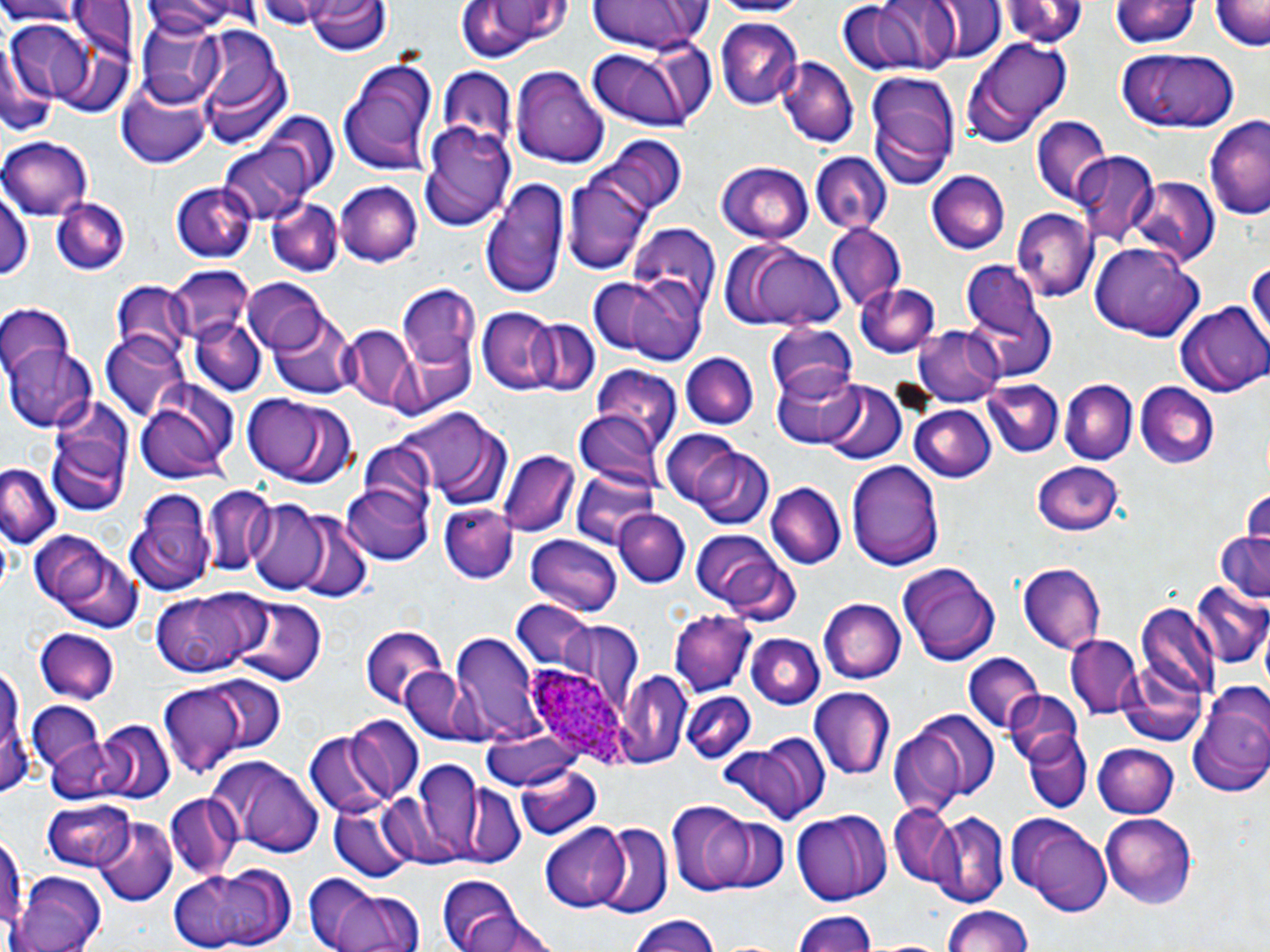
{
  "slide_level_diagnosis": "Plasmodium ovale",
  "magnification": "1000x",
  "plasmodium_ovale_infected_red_blood_cell_locations": "approximate bounding boxes as [x1, y1, x2, y2] in pixels: [526, 665, 626, 764]",
  "image_size": "1270×952 pixels",
  "uninfected_red_blood_cell_locations": "approximate bounding boxes as [x1, y1, x2, y2] in pixels: [0, 0, 86, 25], [258, 0, 322, 32], [583, 0, 715, 54], [703, 0, 813, 17], [839, 0, 963, 77], [136, 1, 258, 37], [305, 1, 389, 56], [450, 1, 570, 64], [932, 1, 1004, 65], [1002, 1, 1088, 51], [1111, 1, 1198, 52], [1212, 2, 1268, 51], [714, 15, 802, 108], [134, 19, 227, 104], [6, 22, 98, 100], [190, 23, 292, 145], [973, 37, 1071, 134], [0, 39, 53, 140], [583, 43, 698, 130], [1114, 48, 1240, 134], [337, 55, 441, 176], [776, 56, 858, 150], [511, 65, 610, 168], [436, 70, 514, 153], [865, 74, 959, 188], [117, 76, 213, 170], [1030, 116, 1112, 204], [1205, 118, 1270, 223], [418, 120, 517, 229], [600, 136, 685, 217], [1, 137, 92, 221], [220, 138, 318, 224], [809, 152, 891, 234], [1076, 153, 1157, 241], [563, 160, 658, 275], [715, 163, 815, 242], [928, 170, 1010, 254], [1129, 176, 1221, 267], [480, 178, 569, 299], [169, 180, 258, 263], [332, 181, 423, 267], [2, 183, 35, 280], [50, 194, 131, 277], [267, 199, 342, 276], [1012, 209, 1096, 302], [825, 224, 905, 308], [629, 226, 720, 310], [719, 238, 848, 332], [1089, 240, 1207, 340], [1248, 250, 1269, 355], [961, 259, 1051, 355], [166, 268, 256, 349], [588, 276, 705, 365], [243, 279, 330, 353], [853, 281, 941, 358], [109, 284, 194, 368], [396, 287, 482, 373], [0, 303, 72, 386], [1175, 303, 1269, 396], [476, 306, 566, 394], [267, 307, 360, 400], [189, 314, 267, 397], [529, 317, 599, 395], [765, 324, 861, 404], [916, 325, 1006, 406], [341, 326, 419, 411], [103, 331, 193, 421], [5, 342, 98, 431], [682, 354, 755, 430], [590, 365, 684, 452], [771, 366, 865, 448], [133, 379, 239, 481], [1061, 379, 1136, 465], [820, 380, 906, 465], [981, 380, 1065, 459], [1134, 381, 1219, 469], [242, 394, 329, 479], [42, 397, 136, 514], [908, 405, 996, 482], [395, 410, 516, 512], [575, 411, 665, 495], [659, 430, 751, 510], [689, 445, 774, 528], [499, 448, 579, 537], [847, 458, 943, 572], [1034, 460, 1124, 534], [0, 465, 60, 547], [573, 472, 660, 545], [342, 480, 435, 566], [766, 482, 845, 569], [201, 484, 279, 577], [126, 486, 239, 594], [1239, 488, 1270, 547], [248, 498, 328, 590], [439, 505, 516, 584], [616, 509, 689, 587], [287, 510, 371, 605], [29, 529, 143, 634], [1214, 529, 1270, 607], [692, 531, 786, 610], [525, 534, 623, 617], [896, 560, 1001, 666], [1017, 564, 1104, 651], [1189, 581, 1270, 672], [149, 591, 265, 678], [228, 597, 324, 688], [511, 599, 595, 674], [819, 599, 905, 683], [1134, 604, 1220, 711], [670, 611, 753, 693], [548, 614, 644, 711], [359, 624, 451, 709], [34, 628, 120, 703], [452, 630, 546, 742], [746, 633, 825, 711], [1066, 635, 1143, 721], [963, 655, 1046, 736], [0, 664, 27, 797], [401, 666, 492, 746], [616, 670, 691, 766], [154, 676, 275, 779], [1187, 680, 1270, 799], [808, 686, 896, 784], [1003, 690, 1081, 768], [680, 692, 755, 761], [26, 703, 107, 777], [911, 709, 1001, 803], [345, 717, 426, 800], [97, 721, 173, 801], [888, 725, 969, 817], [480, 727, 581, 792], [1022, 730, 1092, 812], [304, 732, 394, 819], [44, 734, 136, 804], [722, 737, 829, 825], [1092, 742, 1178, 818], [204, 754, 326, 857], [401, 759, 505, 864], [514, 764, 602, 843], [452, 782, 525, 867], [165, 792, 244, 880], [39, 799, 137, 869], [328, 800, 414, 882], [668, 802, 763, 895], [888, 806, 967, 891], [791, 810, 891, 905], [928, 811, 1007, 904], [1011, 812, 1112, 916], [1100, 813, 1198, 909], [93, 819, 175, 906], [0, 822, 26, 946], [595, 822, 671, 915], [541, 824, 635, 911], [169, 863, 298, 950], [13, 870, 107, 952], [302, 871, 427, 952], [432, 876, 553, 950], [939, 903, 1040, 952], [792, 909, 880, 952], [627, 913, 725, 952]",
  "preparation": "thin blood smear",
  "stain": "May-Grünwald-Giemsa",
  "field_of_view": "one of a larger specimen",
  "modality": "light microscopy"
}